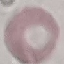
Summary:
  - Malaria status: uninfected
  - Stain: Giemsa
  - Capture: smartphone through the microscope eyepiece
  - Image type: cell patch, automatically extracted from a larger field of view and resized to 64 × 64 pixels
  - Preparation: thin smear